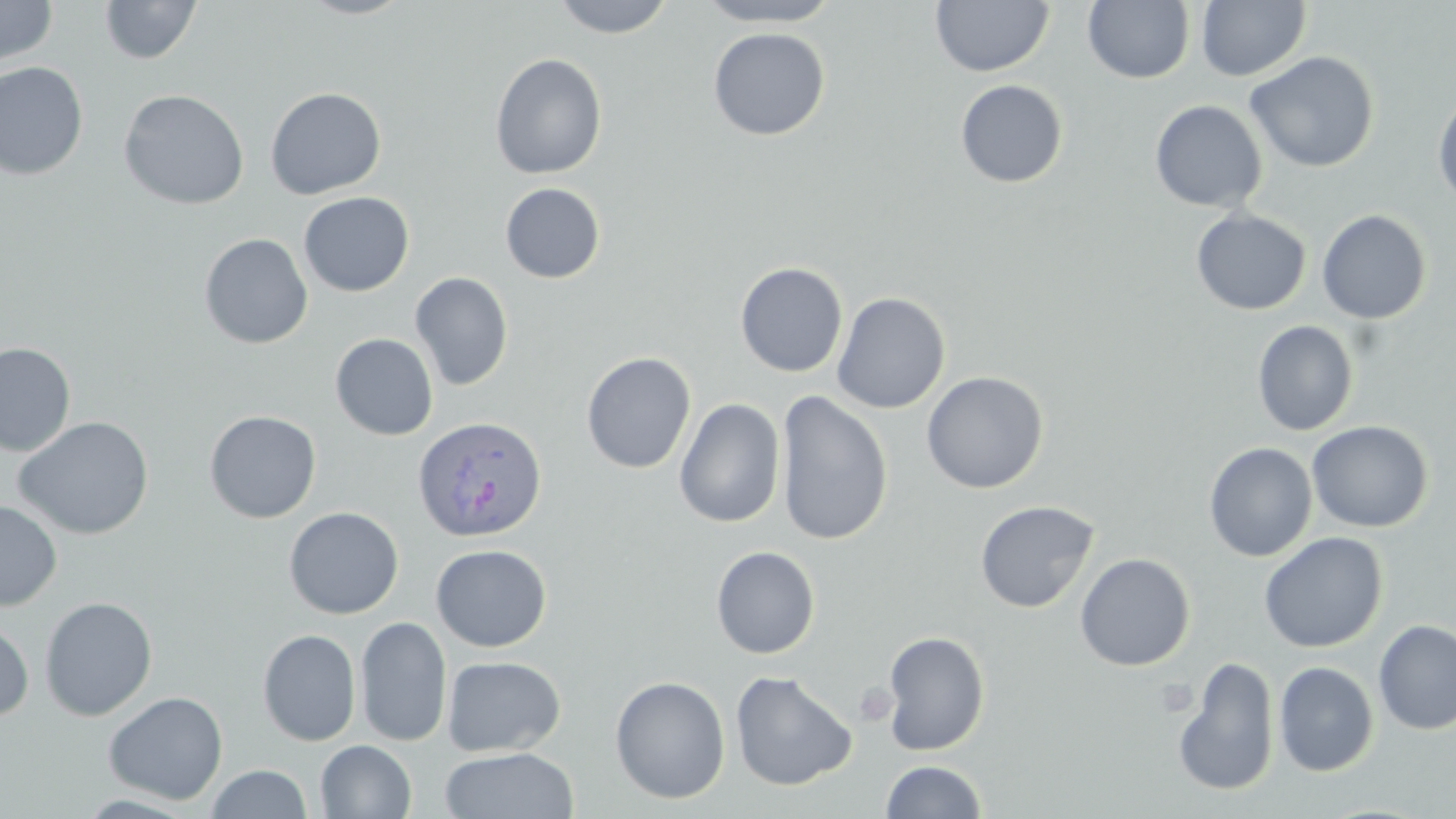

Summary:
  - Coordinate format: approximate bounding boxes as (x1, y1, x2, y2) in pixels
  - Plasmodium ovale-infected red blood cell locations: (412, 415, 547, 542)
  - Platelet locations: (855, 681, 898, 726)
  - Uninfected red blood cell locations: (0, 0, 57, 66), (100, 0, 202, 64), (297, 0, 417, 19), (550, 0, 677, 38), (695, 0, 845, 28), (930, 0, 1054, 77), (1083, 0, 1195, 84), (1197, 1, 1311, 81), (708, 27, 830, 141), (1244, 51, 1380, 173), (490, 53, 608, 179), (0, 61, 89, 180), (955, 79, 1068, 188), (265, 87, 386, 199), (118, 88, 249, 210), (1432, 88, 1456, 209), (1150, 100, 1268, 212), (500, 182, 605, 284), (298, 191, 414, 296), (1191, 208, 1311, 315), (1316, 209, 1432, 324), (199, 233, 313, 349), (735, 262, 848, 377), (410, 272, 513, 391), (831, 292, 950, 414), (1252, 320, 1359, 436), (330, 333, 439, 441), (0, 342, 76, 456), (581, 351, 697, 474), (921, 371, 1049, 494), (775, 391, 893, 546), (674, 397, 786, 528), (204, 410, 322, 523), (13, 416, 154, 540), (1307, 420, 1433, 533), (1204, 442, 1317, 562), (974, 499, 1100, 613), (0, 500, 62, 611), (283, 506, 404, 619), (1258, 532, 1388, 653), (430, 544, 552, 652), (711, 545, 820, 659), (1074, 552, 1195, 671), (39, 596, 158, 721), (355, 616, 452, 747), (0, 617, 34, 722), (1373, 619, 1456, 735), (258, 629, 361, 746), (880, 630, 990, 755), (442, 655, 566, 757), (1173, 657, 1281, 798), (1274, 661, 1379, 777), (730, 670, 858, 791), (609, 675, 731, 804), (103, 690, 228, 805), (315, 740, 416, 818), (439, 747, 579, 819), (879, 760, 988, 818), (206, 764, 312, 819)
  - Slide-level diagnosis: Plasmodium ovale
  - Modality: optical microscopy
  - Preparation: thin blood film
  - Field of view: one of a larger specimen
  - Image size: 1456×819 pixels
  - Stain: May-Grünwald-Giemsa
  - Magnification: 1000x